Classify this cell by malaria status.
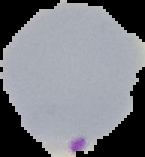
It is parasitized.

Summary:
  - Preparation: thin blood film
  - Image size: 145×157 pixels
  - Image type: segmented cell region on a black background